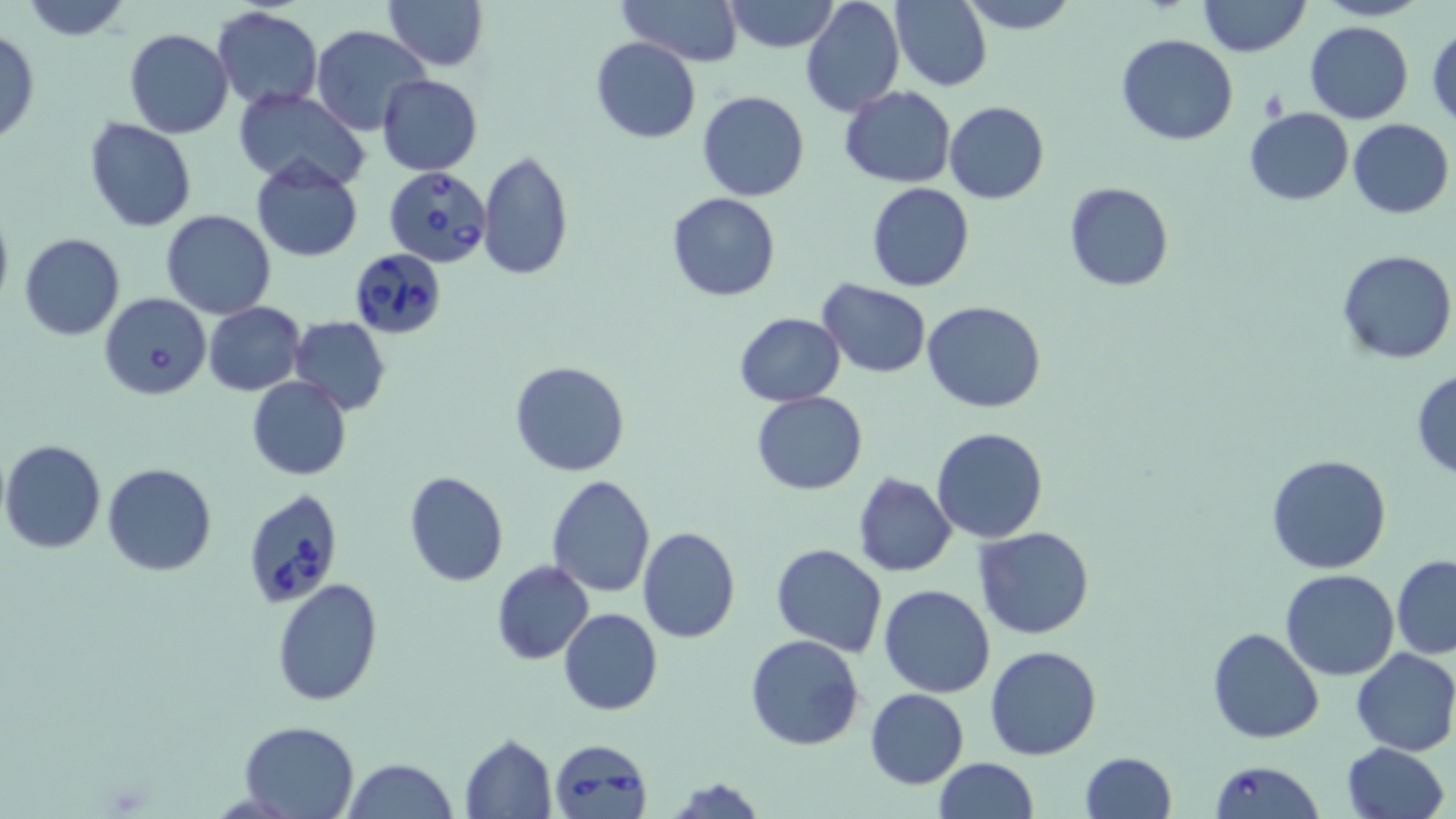
slide_level_diagnosis: Babesia divergens
field_of_view: one of a larger specimen
image_size: 1456×819 pixels
uninfected_red_blood_cell_locations: 'approximate bounding boxes as named x1/y1/x2/y2 corners in pixels: (x1=20, y1=0, x2=132, y2=40), (x1=383, y1=0, x2=486, y2=70), (x1=617, y1=0, x2=743, y2=67), (x1=720, y1=0, x2=840, y2=52), (x1=799, y1=0, x2=905, y2=118), (x1=958, y1=0, x2=1079, y2=34), (x1=1197, y1=0, x2=1311, y2=56), (x1=1312, y1=0, x2=1430, y2=21), (x1=890, y1=1, x2=992, y2=92), (x1=213, y1=5, x2=323, y2=111), (x1=1305, y1=20, x2=1414, y2=123), (x1=311, y1=24, x2=429, y2=134), (x1=1427, y1=24, x2=1456, y2=127), (x1=123, y1=29, x2=233, y2=139), (x1=0, y1=31, x2=40, y2=145), (x1=1116, y1=33, x2=1238, y2=145), (x1=589, y1=37, x2=702, y2=143), (x1=377, y1=75, x2=483, y2=175), (x1=840, y1=85, x2=956, y2=189), (x1=233, y1=89, x2=369, y2=190), (x1=697, y1=89, x2=809, y2=202), (x1=943, y1=102, x2=1049, y2=203), (x1=1244, y1=107, x2=1353, y2=204), (x1=84, y1=118, x2=198, y2=233), (x1=1348, y1=119, x2=1455, y2=220), (x1=475, y1=151, x2=573, y2=282), (x1=251, y1=160, x2=364, y2=263), (x1=1062, y1=181, x2=1174, y2=291), (x1=866, y1=182, x2=974, y2=291), (x1=670, y1=195, x2=785, y2=304), (x1=0, y1=201, x2=14, y2=317), (x1=161, y1=209, x2=276, y2=320), (x1=18, y1=233, x2=125, y2=341), (x1=1336, y1=249, x2=1455, y2=364), (x1=818, y1=279, x2=931, y2=379), (x1=921, y1=300, x2=1046, y2=414), (x1=204, y1=302, x2=305, y2=396), (x1=735, y1=312, x2=845, y2=406), (x1=289, y1=317, x2=391, y2=414), (x1=508, y1=360, x2=632, y2=477), (x1=1410, y1=369, x2=1456, y2=478), (x1=246, y1=375, x2=350, y2=480), (x1=752, y1=391, x2=868, y2=494), (x1=932, y1=428, x2=1049, y2=544), (x1=0, y1=439, x2=107, y2=555), (x1=1265, y1=453, x2=1394, y2=574), (x1=101, y1=462, x2=218, y2=577), (x1=402, y1=471, x2=509, y2=587), (x1=545, y1=473, x2=657, y2=599), (x1=851, y1=473, x2=957, y2=576), (x1=637, y1=526, x2=740, y2=643), (x1=975, y1=526, x2=1094, y2=640), (x1=770, y1=543, x2=888, y2=658), (x1=1392, y1=555, x2=1456, y2=658), (x1=492, y1=561, x2=594, y2=665), (x1=1281, y1=568, x2=1399, y2=679), (x1=270, y1=577, x2=383, y2=706), (x1=879, y1=584, x2=997, y2=698), (x1=559, y1=608, x2=662, y2=716), (x1=1207, y1=627, x2=1325, y2=745), (x1=745, y1=634, x2=865, y2=751), (x1=985, y1=645, x2=1102, y2=761), (x1=1351, y1=647, x2=1456, y2=756), (x1=866, y1=687, x2=968, y2=789), (x1=238, y1=720, x2=361, y2=818), (x1=460, y1=735, x2=557, y2=817), (x1=1340, y1=741, x2=1450, y2=819), (x1=1080, y1=752, x2=1177, y2=819), (x1=934, y1=757, x2=1036, y2=819), (x1=343, y1=758, x2=458, y2=819), (x1=670, y1=775, x2=767, y2=818)'
platelet_locations: 'approximate bounding boxes as named x1/y1/x2/y2 corners in pixels: (x1=1260, y1=88, x2=1290, y2=120)'
babesia_divergens_infected_red_blood_cell_locations: 'approximate bounding boxes as named x1/y1/x2/y2 corners in pixels: (x1=384, y1=165, x2=491, y2=268), (x1=349, y1=248, x2=450, y2=340), (x1=99, y1=292, x2=211, y2=401), (x1=243, y1=488, x2=343, y2=610), (x1=549, y1=737, x2=653, y2=819), (x1=1207, y1=761, x2=1323, y2=818)'
modality: light microscopy
preparation: thin blood film
magnification: 1000x
stain: May-Grünwald-Giemsa